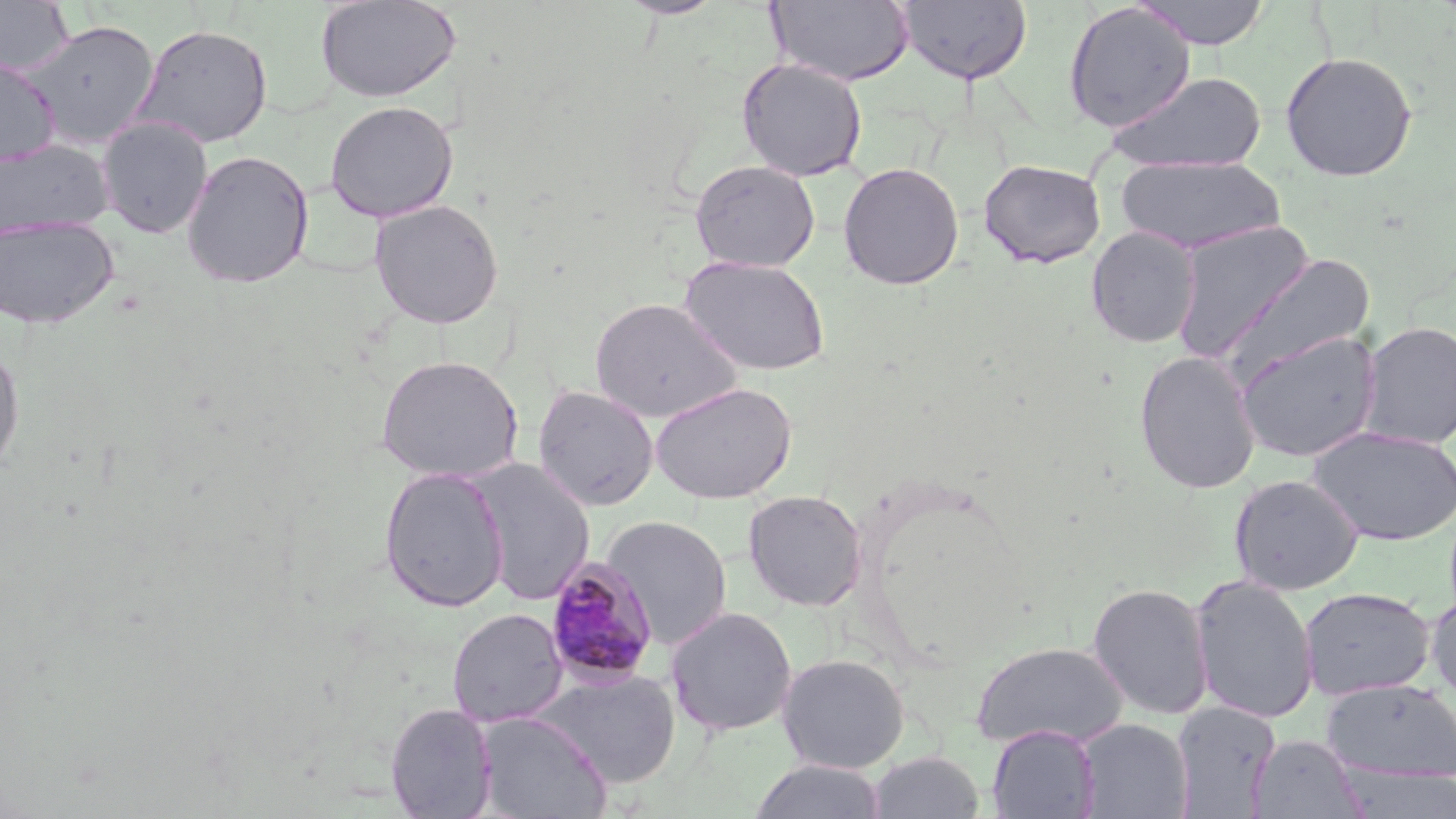
Summary:
  - Coordinate format: approximate bounding boxes as [x1, y1, x2, y2] in pixels
  - Plasmodium malariae-infected red blood cell locations (subset): [544, 558, 660, 688]
  - Uninfected red blood cell locations (subset): [0, 0, 74, 77], [315, 0, 462, 103], [616, 0, 725, 19], [768, 0, 915, 86], [896, 0, 1033, 85], [1133, 0, 1271, 49], [1062, 2, 1196, 133], [22, 20, 160, 149], [132, 23, 273, 148], [1280, 51, 1418, 182], [0, 58, 60, 168], [736, 58, 868, 181], [1104, 71, 1268, 173], [324, 100, 458, 223], [97, 116, 214, 239], [0, 139, 113, 238], [180, 149, 315, 289], [1116, 155, 1285, 255], [688, 159, 821, 273], [978, 159, 1106, 268], [838, 161, 964, 291], [368, 198, 504, 330], [0, 215, 119, 329], [1170, 220, 1316, 362], [1086, 226, 1200, 348], [1220, 253, 1375, 384], [680, 255, 831, 376], [589, 297, 744, 425], [1359, 321, 1456, 449], [1233, 330, 1383, 462], [0, 342, 24, 479], [1134, 350, 1262, 494], [374, 355, 524, 484], [650, 381, 797, 505], [533, 385, 659, 512], [1308, 426, 1456, 546], [378, 465, 509, 612], [1229, 474, 1364, 595], [742, 490, 867, 611], [601, 514, 733, 650], [1190, 575, 1320, 724], [1087, 582, 1214, 720], [1299, 588, 1436, 700], [1426, 591, 1456, 705], [664, 606, 798, 736], [447, 608, 568, 727], [971, 640, 1128, 750], [776, 653, 910, 773], [534, 669, 683, 788], [1321, 678, 1456, 782], [1172, 701, 1281, 818], [385, 702, 498, 818], [474, 711, 611, 818], [1076, 718, 1193, 819], [987, 725, 1100, 818], [1248, 734, 1368, 818], [867, 751, 985, 818], [748, 759, 887, 819]
  - Slide-level diagnosis: Plasmodium malariae
  - Modality: light microscopy
  - Stain: May-Grünwald-Giemsa
  - Image size: 1456×819 pixels
  - Field of view: one of a larger specimen
  - Magnification: 1000x
  - Preparation: thin blood smear